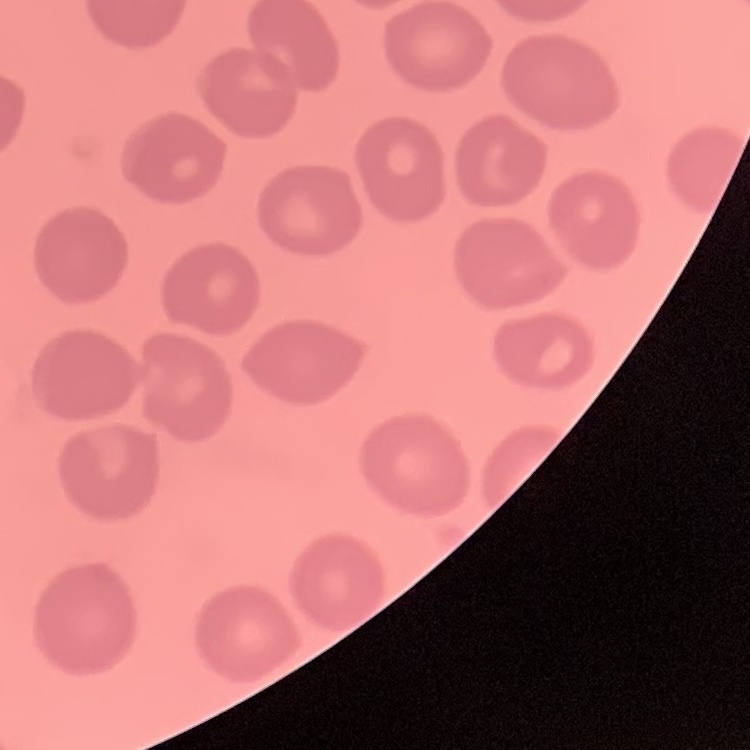
The red blood cells show no rouleaux formation. One tile cut from a larger photomicrograph. Thin blood smear. Stained with either Field's or Giemsa.